Mark where platelets are.
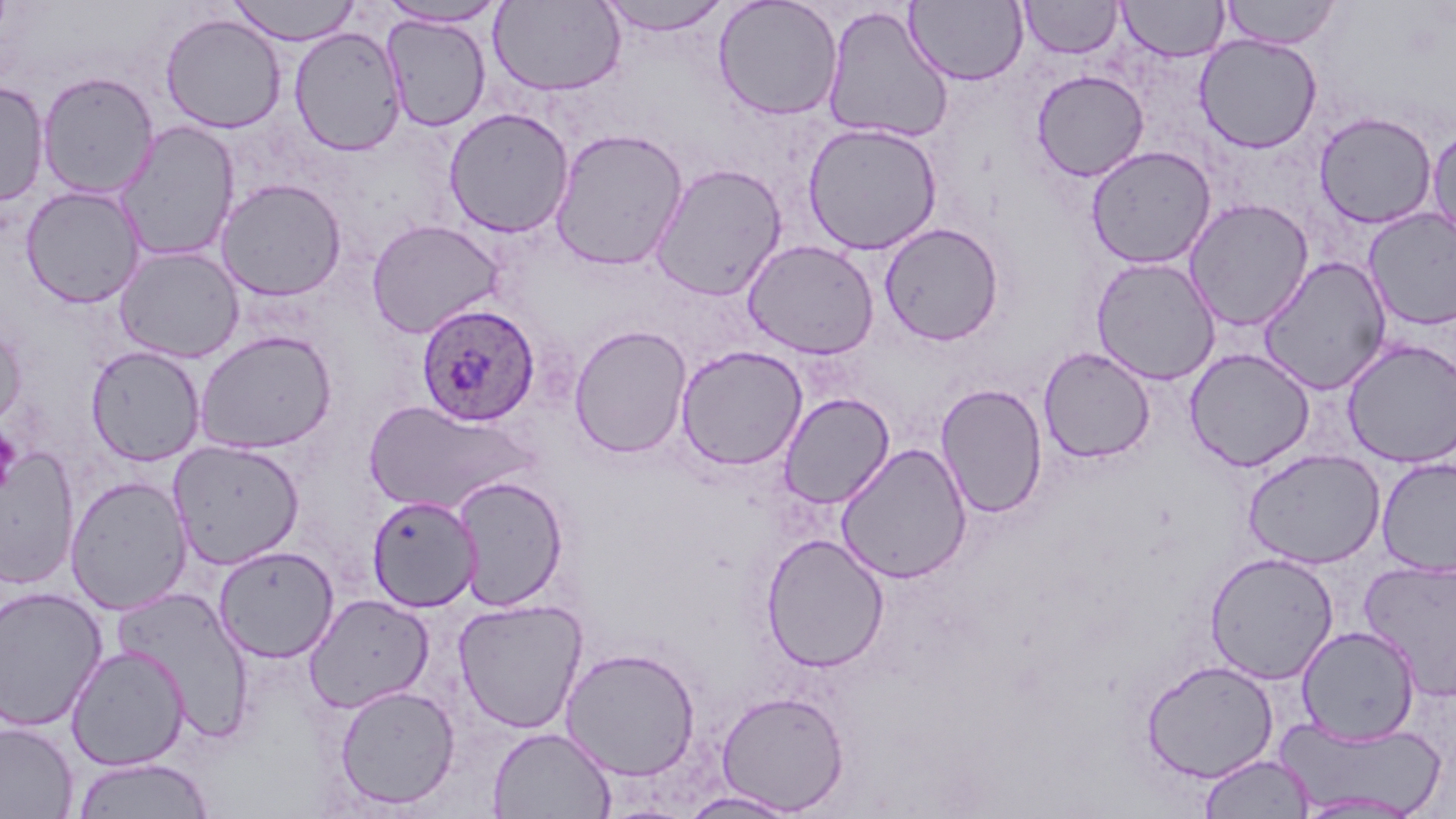

Approximate bounding boxes as (x1, y1, x2, y2) in pixels.
Platelets: (0, 423, 21, 498).

Summary:
  - Uninfected red blood cell locations: (227, 0, 362, 45), (489, 0, 625, 96), (713, 0, 843, 120), (905, 0, 1028, 86), (1019, 0, 1122, 58), (1119, 0, 1229, 61), (376, 1, 509, 27), (598, 1, 732, 36), (1221, 1, 1341, 49), (821, 5, 953, 143), (160, 13, 287, 134), (381, 15, 491, 131), (289, 27, 407, 156), (1195, 34, 1322, 154), (1031, 70, 1148, 181), (37, 71, 159, 199), (0, 80, 50, 206), (443, 107, 575, 238), (1314, 111, 1437, 229), (114, 121, 240, 263), (803, 122, 943, 255), (1428, 125, 1456, 244), (549, 128, 688, 271), (1086, 145, 1216, 269), (650, 162, 787, 301), (216, 178, 347, 301), (21, 186, 146, 308), (1184, 197, 1315, 332), (1363, 207, 1456, 329), (366, 219, 504, 338), (879, 222, 1004, 346), (743, 239, 879, 359), (114, 245, 245, 363), (1090, 256, 1222, 385), (1258, 256, 1392, 395), (0, 320, 26, 431), (569, 324, 692, 459), (194, 330, 337, 454), (1342, 338, 1456, 468), (675, 344, 808, 472), (85, 345, 206, 466), (1038, 346, 1156, 463), (1184, 347, 1315, 472), (935, 383, 1048, 519), (778, 392, 895, 509), (364, 400, 533, 516), (169, 440, 305, 570), (836, 442, 972, 584), (0, 447, 78, 589), (1242, 448, 1386, 568), (1376, 457, 1456, 577), (64, 475, 192, 615), (451, 475, 569, 611), (367, 494, 481, 612), (760, 533, 889, 672), (213, 545, 339, 663), (1204, 551, 1339, 683), (1360, 559, 1456, 700), (0, 586, 108, 731), (111, 587, 254, 742), (304, 593, 434, 712), (453, 598, 588, 734), (1297, 625, 1420, 744), (66, 644, 190, 770), (561, 646, 701, 781), (1141, 659, 1280, 782), (333, 684, 461, 810), (715, 691, 849, 814), (1275, 718, 1445, 817), (0, 722, 78, 819), (487, 725, 616, 819), (1199, 753, 1314, 819), (71, 756, 214, 819), (678, 790, 802, 818), (1293, 791, 1427, 818)
  - Plasmodium ovale-infected red blood cell locations: (416, 302, 541, 427)
  - Slide-level diagnosis: Plasmodium ovale
  - Image size: 1456×819 pixels
  - Stain: May-Grünwald-Giemsa
  - Modality: optical microscopy
  - Preparation: thin blood smear
  - Magnification: 1000x
  - Field of view: single